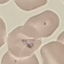 Malaria status: parasitized. Automatically extracted cell patch, resized to 64 × 64 pixels. Photographed with a smartphone camera at the microscope eyepiece. Giemsa-stained preparation. Thin blood film.